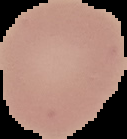 From a thin blood smear. Cell region segmented out of the field of view; the surrounding area is masked to black. Image is 127×139 pixels. Result: negative for malaria parasites.